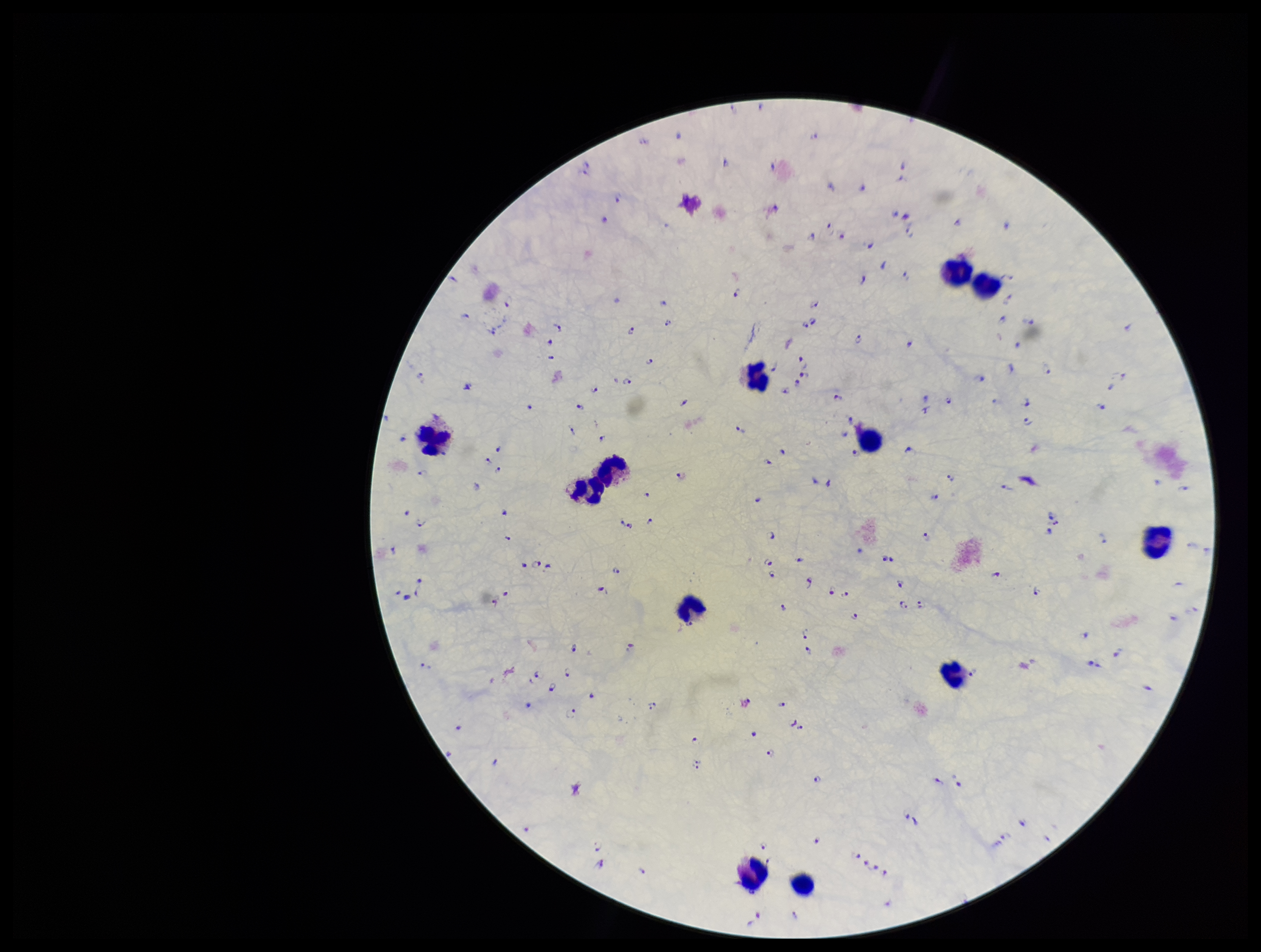

Summary:
  - Parasite count: 181
  - Preparation: thick
  - Image size: 1261×952 pixels
  - Leukocyte count: 12
  - Capture: smartphone photograph through the microscope eyepiece
  - Field of view: one from this slide
  - Species reported for this patient: Plasmodium falciparum
  - Stain: Giemsa
  - Plasmodium parasites: identified
  - Patient malaria status: infected